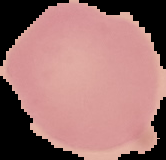
Malaria status: uninfected. From a thin blood film. Image is 166×160 pixels. Cell region segmented out of the field of view; the surrounding area is masked to black.